Identify the parasite.
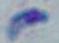

Toxoplasma gondii.

Captured at 1000x magnification. Micrograph.